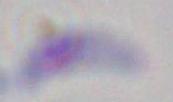
identification = Toxoplasma gondii
modality = photomicrograph
magnification = 1000x